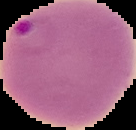

preparation: thin blood film
malaria_status: parasitized
image_type: segmented cell region on a black background
image_size: 136×130 pixels